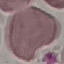
Summary:
  - Result: negative for malaria parasites
  - Capture: smartphone through the microscope eyepiece
  - Stain: Giemsa
  - Image type: cell patch, automatically extracted from a larger field of view and resized to 64 × 64 pixels
  - Preparation: thin blood smear